State which parasite is depicted.
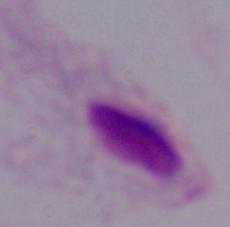
This is a trichomonad.

modality = micrograph
magnification = 1000x